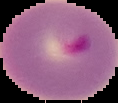

Summary:
  - Preparation: thin blood film
  - Result: malaria parasites detected
  - Image type: segmented cell region with the area outside set to black
  - Image size: 118×103 pixels